Name the blood parasite species.
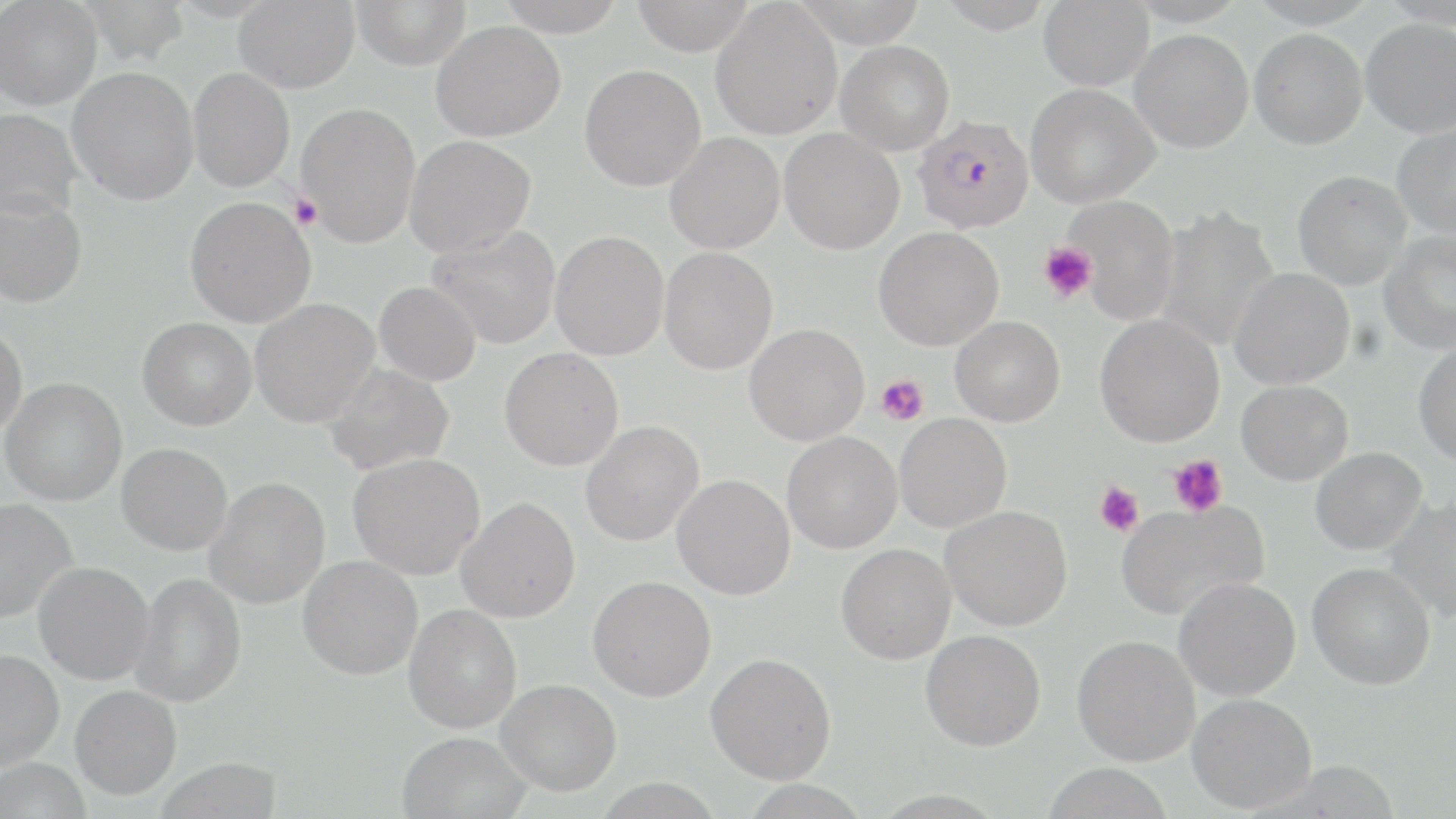
Plasmodium falciparum.

Approximate bounding boxes as [x1, y1, x2, y2] in pixels. Platelet locations: [290, 194, 322, 229], [1038, 242, 1096, 302], [876, 375, 929, 425], [1168, 454, 1227, 517], [1095, 482, 1144, 537]. Uninfected red blood cell locations: [74, 0, 190, 66], [233, 0, 359, 94], [350, 0, 471, 71], [494, 0, 627, 37], [631, 0, 755, 56], [790, 0, 928, 48], [1038, 0, 1154, 90], [1129, 0, 1248, 27], [1246, 0, 1378, 28], [1380, 0, 1456, 29], [0, 1, 103, 110], [710, 1, 842, 140], [1361, 18, 1456, 138], [430, 20, 566, 142], [1249, 28, 1368, 149], [1129, 29, 1254, 153], [835, 41, 955, 154], [579, 64, 706, 191], [67, 67, 199, 206], [188, 68, 295, 192], [1026, 84, 1160, 208], [296, 102, 421, 247], [0, 108, 81, 222], [1392, 125, 1456, 239], [779, 128, 904, 254], [664, 133, 784, 254], [404, 135, 535, 257], [1292, 170, 1412, 290], [0, 193, 88, 308], [1062, 195, 1180, 326], [185, 197, 316, 328], [1154, 206, 1280, 351], [427, 224, 561, 349], [874, 226, 1003, 350], [1378, 230, 1456, 355], [550, 231, 669, 360], [659, 247, 778, 375], [1228, 268, 1355, 390], [374, 282, 481, 386], [250, 298, 379, 427], [1095, 314, 1225, 447], [950, 316, 1066, 426], [137, 317, 256, 430], [0, 323, 27, 438], [744, 323, 870, 445], [1413, 344, 1456, 466], [499, 348, 623, 471], [324, 363, 454, 475], [1, 377, 127, 506], [1236, 380, 1353, 485], [895, 413, 1012, 533], [580, 421, 704, 546], [782, 432, 902, 554], [116, 443, 233, 556], [1310, 447, 1427, 555], [347, 453, 485, 580], [672, 474, 795, 600], [205, 477, 331, 609], [1385, 496, 1456, 623], [456, 497, 580, 623], [0, 498, 77, 624], [1115, 501, 1268, 620], [941, 505, 1073, 631], [836, 543, 956, 665], [297, 555, 423, 680], [33, 561, 154, 685], [1307, 562, 1436, 690], [130, 572, 246, 708], [587, 575, 716, 702], [1173, 577, 1301, 701], [403, 605, 522, 734], [920, 629, 1046, 751], [1072, 635, 1201, 766], [0, 648, 64, 773], [705, 652, 836, 784], [496, 678, 621, 796], [70, 685, 182, 800], [1186, 693, 1317, 813], [397, 731, 532, 819], [1, 757, 91, 818], [1041, 763, 1173, 819]. Plasmodium falciparum-infected red blood cell locations: [913, 115, 1034, 233]. Thin blood smear. 1000x magnification. Image is 1456×819 pixels. One field of a larger specimen. May-Grünwald-Giemsa stain. Light microscopy.